Locate leukocytes (white blood cells).
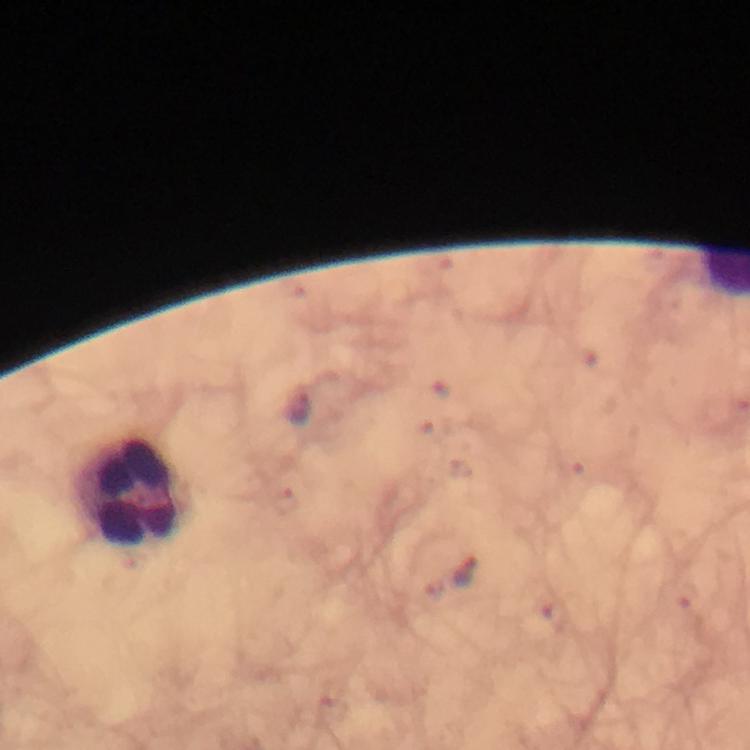

Approximate centers as (x, y) in pixels.
Leukocytes: (129, 490).

{
  "capture": "smartphone mounted on the microscope",
  "preparation": "thick blood film",
  "cropped_from": "a single field of view",
  "magnification": "100x",
  "plasmodium_parasite_locations": "approximate centers as (x, y) in pixels: (465, 573)",
  "stain": "Giemsa",
  "immersion_oil": "used",
  "context": "from a diagnostic examination for malaria",
  "image_size": "750×750 pixels"
}